Name the cell type shown.
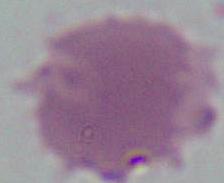

An erythrocyte.

{
  "modality": "micrograph",
  "magnification": "1000x"
}